Describe the morphology of the red blood cells.
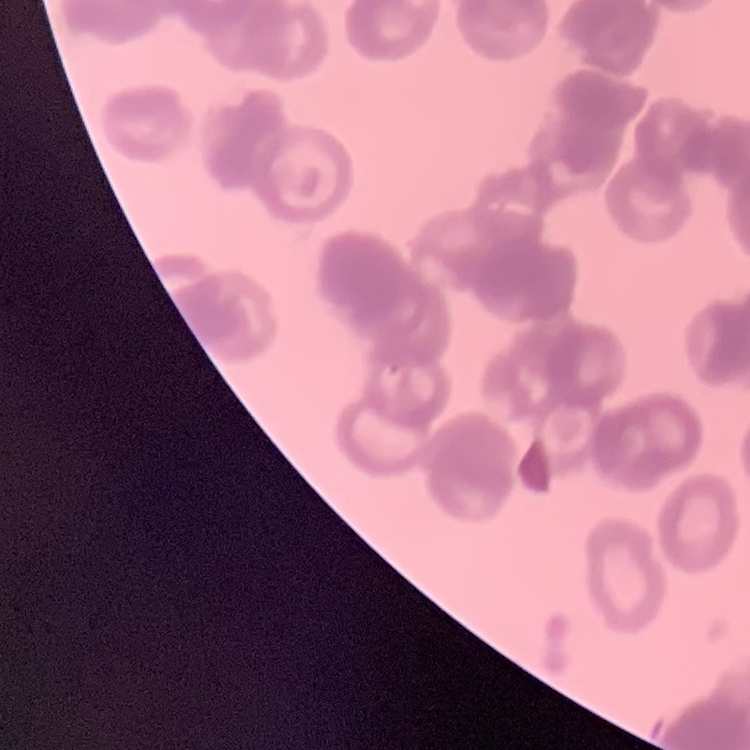

Rouleaux formation.

Summary:
  - Preparation: thin blood smear
  - Image type: one tile cut from a larger photomicrograph
  - Stain: Field's or Giemsa